Outline each uninfected red blood cell.
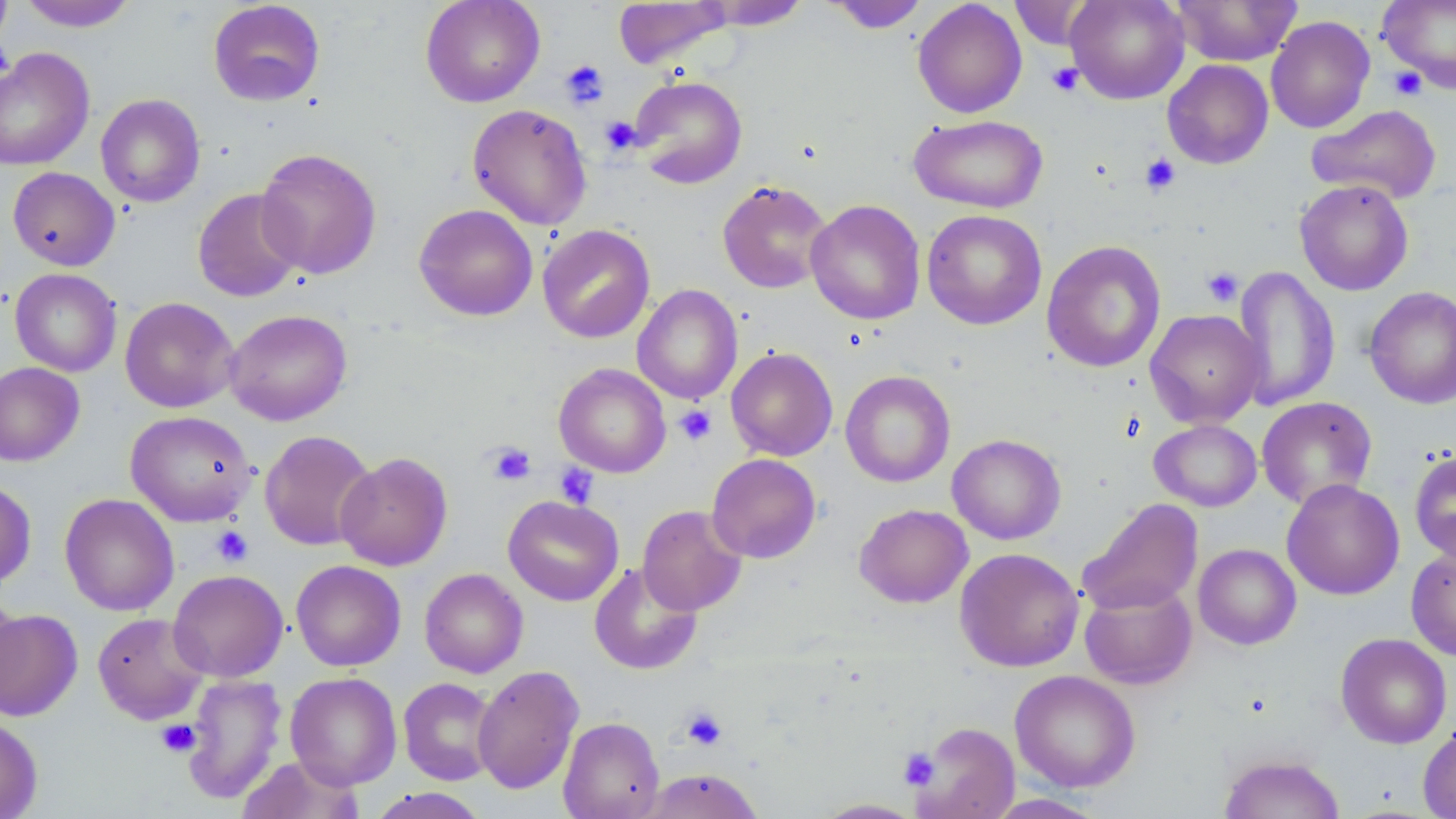

Approximate bounding boxes as (x1,y1)-(x2,y2) corner pairs in pixels.
Uninfected red blood cells: (18,0)-(136,31), (420,0)-(545,107), (826,0)-(929,33), (912,0)-(1028,118), (1009,0)-(1099,50), (1065,0)-(1190,104), (1171,0)-(1301,66), (1378,0)-(1456,93), (208,1)-(325,106), (613,1)-(731,69), (698,1)-(810,31), (1265,15)-(1375,133), (0,48)-(95,171), (1162,59)-(1274,169), (629,75)-(747,188), (96,93)-(205,208), (1306,103)-(1442,204), (467,104)-(593,230), (909,114)-(1048,213), (255,148)-(382,279), (8,167)-(120,271), (1294,179)-(1413,296), (717,180)-(833,294), (193,188)-(305,302), (805,198)-(926,325), (414,204)-(538,321), (921,209)-(1047,330), (537,224)-(655,343), (1041,240)-(1166,372), (1232,265)-(1340,411), (10,268)-(122,377), (632,284)-(742,404), (1364,285)-(1456,409), (120,297)-(239,413), (225,309)-(352,425), (1145,309)-(1265,428), (726,346)-(838,461), (0,362)-(85,466), (553,363)-(671,477), (840,370)-(955,488), (1256,396)-(1378,510), (125,411)-(256,526), (1149,419)-(1262,512), (259,430)-(377,551), (947,434)-(1066,545), (1409,449)-(1456,564), (335,452)-(453,570), (706,454)-(821,563), (1281,479)-(1404,600), (0,480)-(36,589), (59,493)-(179,616), (502,495)-(624,606), (1078,498)-(1203,616), (854,503)-(973,608), (637,505)-(747,615), (1193,544)-(1301,650), (1406,547)-(1456,661), (955,548)-(1084,671), (290,560)-(406,671), (588,562)-(703,675), (419,568)-(528,678), (168,569)-(288,682), (1080,582)-(1197,690), (0,589)-(22,705), (0,608)-(83,721), (92,612)-(208,724), (1335,632)-(1452,749), (472,665)-(584,795), (1010,670)-(1140,792), (286,672)-(402,789), (182,674)-(287,805), (398,677)-(500,785), (0,715)-(43,819), (558,716)-(665,819), (911,722)-(1020,819), (1418,725)-(1456,819), (1218,753)-(1345,818), (236,755)-(365,819), (637,768)-(765,819), (366,787)-(491,818), (981,794)-(1109,818), (814,798)-(925,818).

slide_level_diagnosis: negative for blood parasites
magnification: 1000x
field_of_view: one of a larger specimen
preparation: thin blood smear
image_size: 1456×819 pixels
stain: May-Grünwald-Giemsa
platelet_locations: 'approximate bounding boxes as (x1,y1)-(x2,y2) corner pairs in pixels: (560,59)-(609,109), (1046,62)-(1084,96), (1387,66)-(1427,101), (600,116)-(642,154), (1139,153)-(1181,195), (1201,266)-(1243,307), (675,404)-(717,445), (486,442)-(536,486), (555,463)-(599,508), (211,526)-(253,566), (680,706)-(728,750), (156,719)-(200,757), (899,748)-(940,790)'
modality: light microscopy